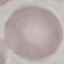

Result: negative for malaria parasites. Cell patch, automatically extracted from a larger field of view and resized to 64 × 64 pixels. Thin smear of blood. Giemsa-stained preparation. Photographed with a smartphone camera at the microscope eyepiece.